Give the position of every Plasmodium parasite.
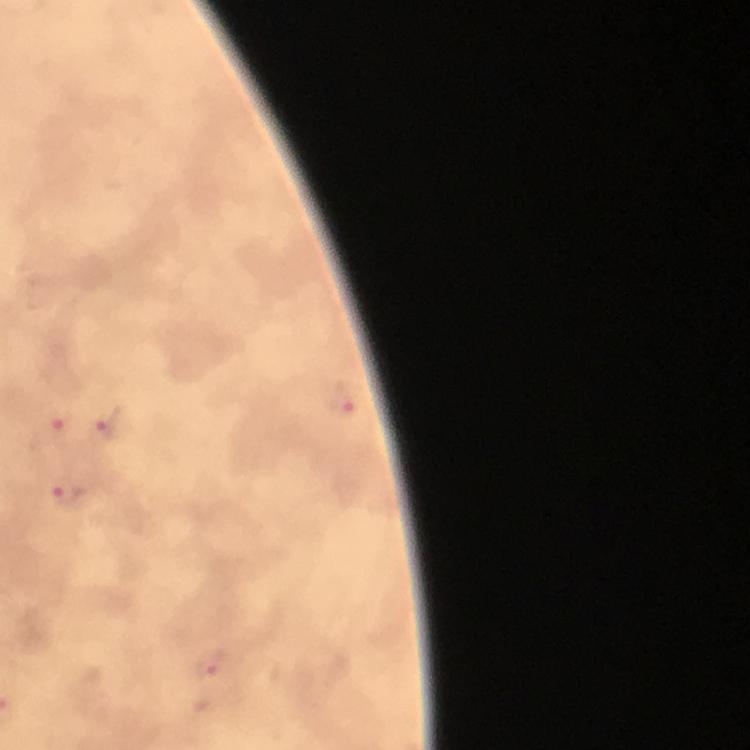
Approximate centers as {x, y} in pixels.
Plasmodium parasites: {345, 406}, {106, 425}, {57, 427}, {66, 495}, {211, 669}.

context: from a malaria diagnostic workup
cropped_from: one field of view
magnification: 100x
immersion_oil: used
preparation: thick blood film
image_size: 750×750 pixels
capture: smartphone camera through the microscope
stain: Giemsa